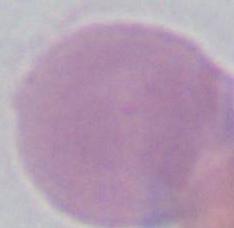

modality: micrograph
identification: erythrocyte
magnification: 1000x